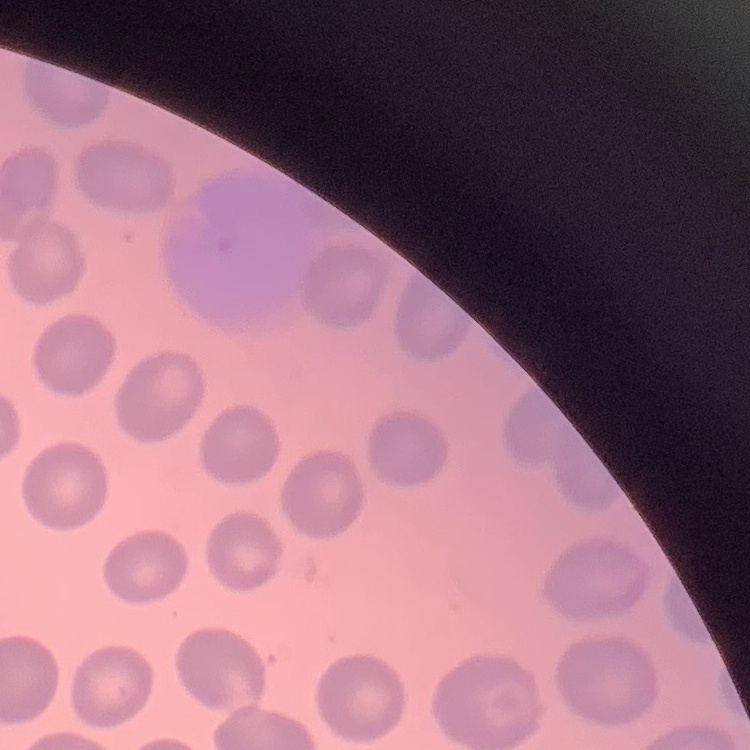
erythrocyte morphology = no rouleaux formation
image type = one tile cut from a larger photomicrograph
preparation = thin blood smear
stain = Field's or Giemsa